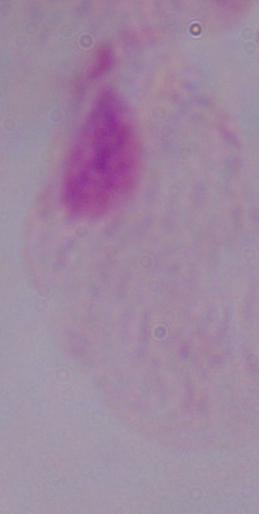 Photomicrograph. 1000x magnification. A trichomonad is seen.